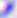 Toxoplasma gondii is shown. Captured at 400x magnification. Photomicrograph.